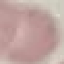

Malaria status: uninfected. Giemsa stain. Thin blood smear. Photographed with a smartphone camera at the microscope eyepiece. Automatically extracted cell patch, resized to 64 × 64 pixels.